Name the blood parasite species.
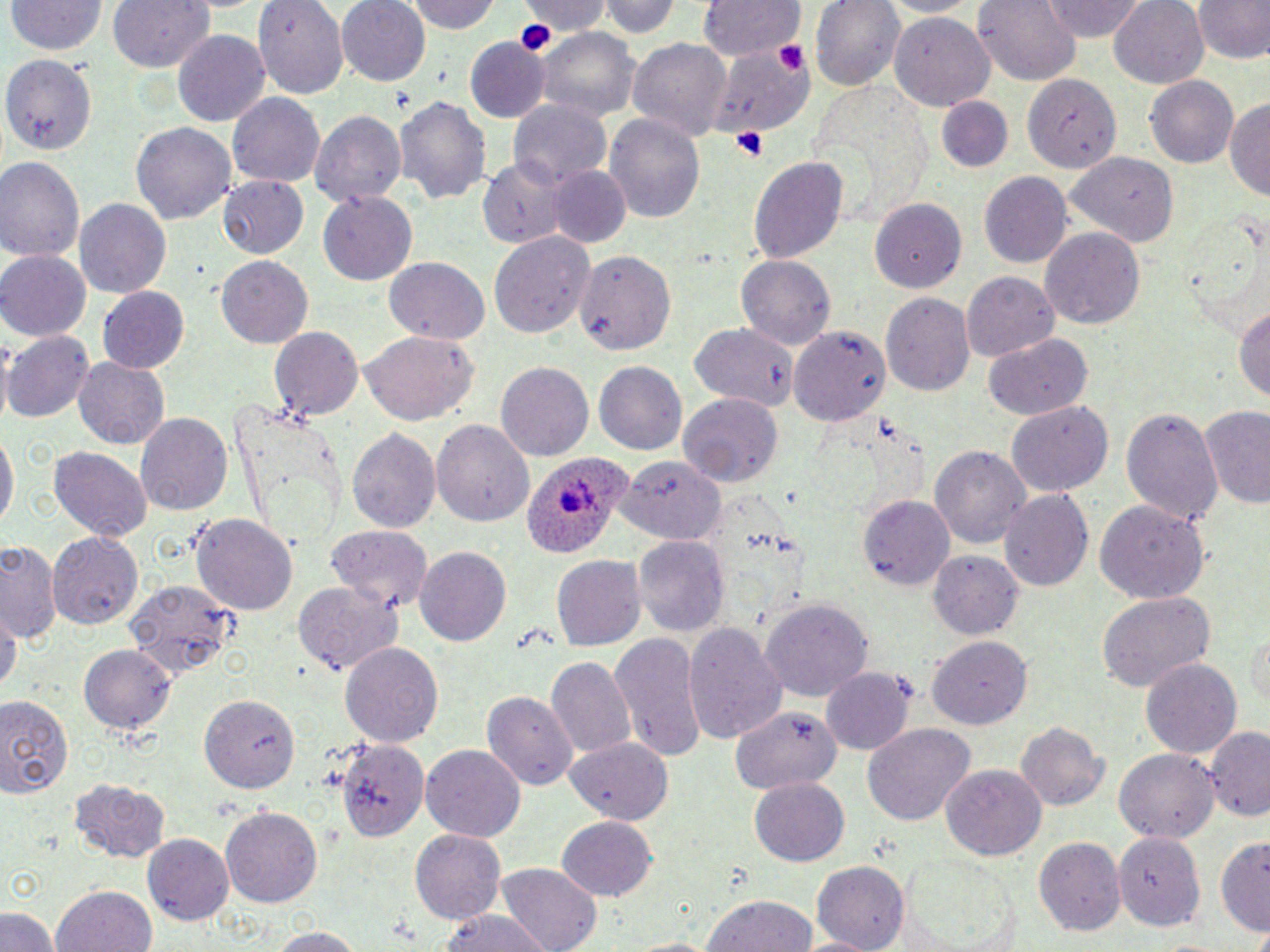

Plasmodium ovale.

Summary:
  - Coordinate format: approximate bounding boxes as (x1, y1, x2, y2) in pixels
  - Platelet locations: (517, 21, 554, 50), (780, 39, 811, 75), (729, 128, 770, 160)
  - Uninfected red blood cell locations: (8, 0, 105, 56), (107, 0, 215, 73), (337, 0, 432, 87), (406, 0, 502, 35), (519, 0, 608, 39), (602, 0, 680, 39), (699, 0, 803, 60), (809, 0, 907, 90), (880, 0, 979, 17), (974, 0, 1081, 86), (1039, 0, 1148, 40), (1189, 0, 1270, 64), (1108, 1, 1209, 88), (253, 2, 349, 100), (890, 10, 995, 108), (535, 31, 640, 120), (174, 33, 270, 124), (710, 36, 817, 143), (628, 38, 734, 144), (465, 41, 547, 122), (1, 50, 97, 154), (1026, 75, 1119, 174), (1146, 75, 1239, 169), (228, 93, 325, 188), (394, 94, 492, 207), (1225, 96, 1270, 199), (935, 98, 1015, 175), (509, 101, 611, 190), (310, 110, 407, 208), (605, 113, 706, 225), (132, 120, 235, 222), (1065, 152, 1177, 246), (0, 156, 85, 263), (747, 156, 850, 264), (479, 157, 574, 247), (549, 164, 629, 248), (978, 173, 1071, 268), (220, 175, 309, 257), (319, 193, 417, 284), (73, 197, 171, 299), (869, 198, 966, 292), (1040, 228, 1145, 331), (487, 230, 596, 341), (0, 251, 90, 339), (574, 251, 677, 356), (736, 252, 836, 349), (216, 254, 312, 346), (385, 255, 489, 344), (961, 269, 1058, 360), (98, 288, 189, 373), (881, 292, 975, 399), (1234, 299, 1270, 406), (689, 323, 796, 409), (790, 324, 890, 424), (270, 325, 366, 423), (360, 330, 475, 427), (4, 331, 94, 421), (984, 333, 1094, 421), (73, 356, 170, 450), (497, 362, 593, 462), (594, 362, 686, 456), (677, 393, 783, 487), (1006, 401, 1113, 498), (1120, 406, 1225, 529), (1199, 406, 1270, 511), (135, 413, 232, 517), (433, 418, 536, 531), (0, 428, 16, 536), (348, 429, 439, 535), (931, 445, 1032, 550), (49, 446, 153, 542), (617, 455, 725, 542), (998, 487, 1094, 592), (860, 493, 957, 590), (1094, 496, 1209, 603), (193, 514, 299, 617), (327, 527, 431, 611), (48, 533, 145, 630), (635, 538, 729, 635), (0, 543, 61, 641), (415, 547, 511, 648), (930, 549, 1023, 638), (550, 551, 644, 649), (125, 581, 238, 676), (292, 582, 400, 679), (1096, 590, 1215, 693), (761, 596, 870, 702), (2, 604, 19, 697), (685, 623, 785, 742), (1248, 628, 1270, 720), (610, 633, 706, 761), (928, 634, 1033, 725), (79, 642, 180, 732), (342, 642, 442, 751), (547, 656, 637, 760), (1141, 657, 1243, 760), (820, 669, 913, 756), (483, 691, 577, 790), (202, 693, 300, 791), (0, 695, 74, 801), (731, 706, 841, 793), (1016, 721, 1110, 811), (862, 725, 976, 826), (1205, 726, 1269, 819), (562, 737, 676, 824), (336, 738, 427, 844), (421, 743, 525, 840), (1114, 748, 1219, 842), (941, 763, 1046, 860), (71, 777, 171, 861), (749, 777, 848, 867), (221, 807, 323, 907), (556, 815, 659, 902), (410, 829, 506, 924), (1115, 831, 1207, 930), (143, 832, 236, 925), (1216, 834, 1270, 935), (1033, 835, 1124, 936), (901, 856, 1020, 951), (498, 861, 601, 952), (811, 862, 909, 949), (52, 886, 157, 952), (701, 894, 821, 951), (2, 907, 56, 952), (434, 908, 553, 952), (266, 927, 367, 952)
  - Plasmodium ovale-infected red blood cell locations: (520, 450, 641, 563)
  - Modality: optical microscopy
  - Stain: May-Grünwald-Giemsa
  - Image size: 1270×952 pixels
  - Preparation: thin blood smear
  - Magnification: 1000x
  - Field of view: single